Name the parasite shown.
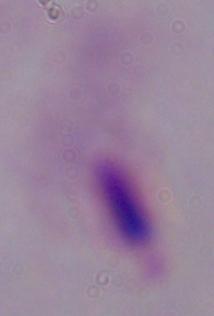

A trichomonad.

Summary:
  - Magnification: 1000x
  - Modality: photomicrograph